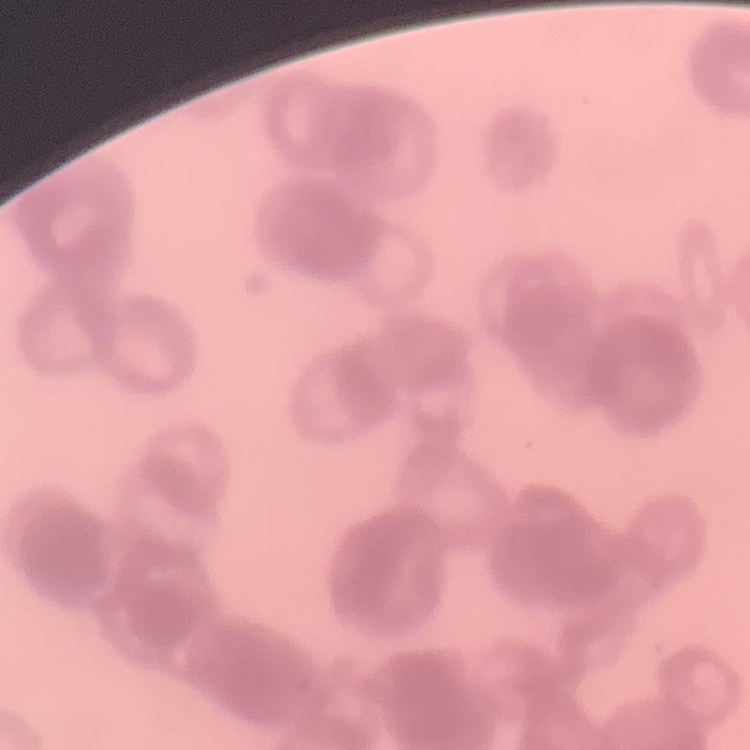

Summary:
  - Erythrocyte morphology: rouleaux formation
  - Image type: square crop of a larger photomicrograph
  - Stain: Field's or Giemsa
  - Preparation: thin peripheral smear